Comment on the morphology of the red blood cells.
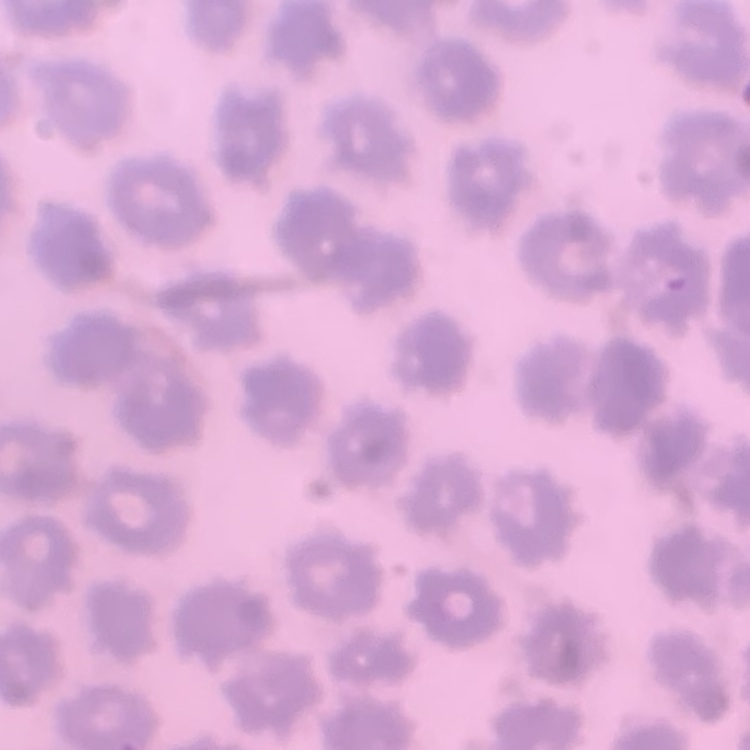
No rouleaux formation.

Thin blood film. Square crop of a larger photomicrograph. Stained with either Field's or Giemsa.